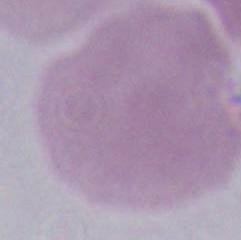

Summary:
  - Identification: erythrocyte
  - Magnification: 1000x
  - Modality: micrograph